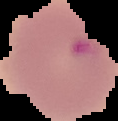
Summary:
  - Result: no Plasmodium parasites detected
  - Preparation: thin blood film
  - Image type: cell region segmented out of the field of view; surrounding area masked to black
  - Image size: 118×121 pixels